Give the extent of all uninfected red blood cells.
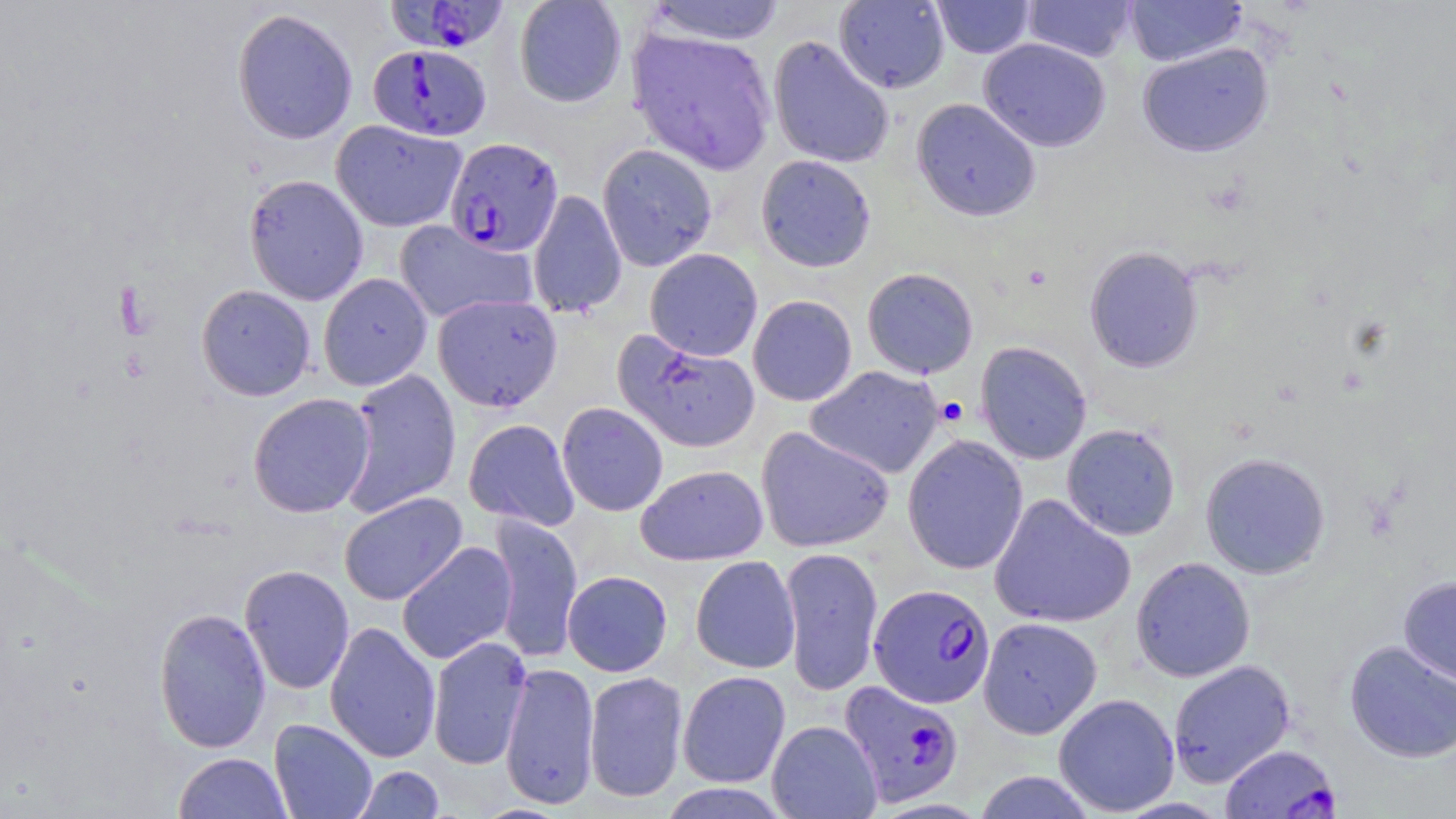

Approximate bounding boxes as (x1,y1)-(x2,y2) corner pairs in pixels.
Uninfected red blood cells: (513,0)-(627,108), (834,0)-(950,93), (932,0)-(1035,58), (1124,0)-(1248,67), (643,1)-(786,46), (1023,1)-(1137,62), (231,8)-(359,145), (628,27)-(777,174), (768,36)-(894,169), (978,37)-(1111,152), (1137,42)-(1273,157), (912,98)-(1041,222), (330,120)-(467,232), (597,143)-(718,272), (755,154)-(876,272), (243,174)-(369,306), (527,189)-(626,318), (393,220)-(538,324), (1084,246)-(1204,373), (645,248)-(763,361), (862,267)-(979,379), (318,272)-(432,391), (196,284)-(316,401), (432,294)-(563,412), (748,295)-(857,406), (614,332)-(760,453), (975,341)-(1092,464), (806,365)-(944,479), (340,369)-(462,518), (248,393)-(375,518), (557,402)-(668,517), (463,418)-(580,531), (1061,423)-(1181,540), (755,427)-(895,553), (902,435)-(1028,575), (1200,452)-(1331,579), (636,464)-(768,565), (338,492)-(467,606), (988,493)-(1135,629), (487,513)-(583,664), (396,541)-(518,664), (780,546)-(884,697), (690,555)-(801,674), (1131,557)-(1256,682), (239,564)-(355,695), (562,570)-(673,676), (1398,575)-(1456,689), (153,607)-(271,753), (977,616)-(1102,739), (324,621)-(441,763), (427,636)-(532,770), (1344,640)-(1456,763), (1167,659)-(1295,787), (499,662)-(600,809), (677,670)-(791,788), (583,671)-(689,803), (1053,693)-(1180,816), (269,719)-(378,819), (766,720)-(882,818), (174,752)-(292,818), (353,766)-(445,818), (973,771)-(1097,818), (656,783)-(793,818).

{
  "slide_level_diagnosis": "Plasmodium falciparum",
  "preparation": "thin blood smear",
  "image_size": "1456×819 pixels",
  "modality": "optical microscopy",
  "stain": "May-Grünwald-Giemsa",
  "magnification": "1000x",
  "platelet_locations": "approximate bounding boxes as (x1,y1)-(x2,y2) corner pairs in pixels: (936,397)-(969,428)",
  "field_of_view": "single",
  "plasmodium_falciparum_infected_red_blood_cell_locations": "approximate bounding boxes as (x1,y1)-(x2,y2) corner pairs in pixels: (386,0)-(510,54), (368,44)-(491,142), (445,137)-(563,256), (869,583)-(996,709), (839,680)-(965,807), (1219,743)-(1340,818)"
}